Classify this cell by malaria status.
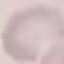
It is uninfected.

{
  "image_type": "cell patch, automatically extracted from a larger field of view and resized to 64 × 64 pixels",
  "preparation": "thin blood smear",
  "stain": "Giemsa",
  "capture": "smartphone through the microscope eyepiece"
}